Comment on the background quality.
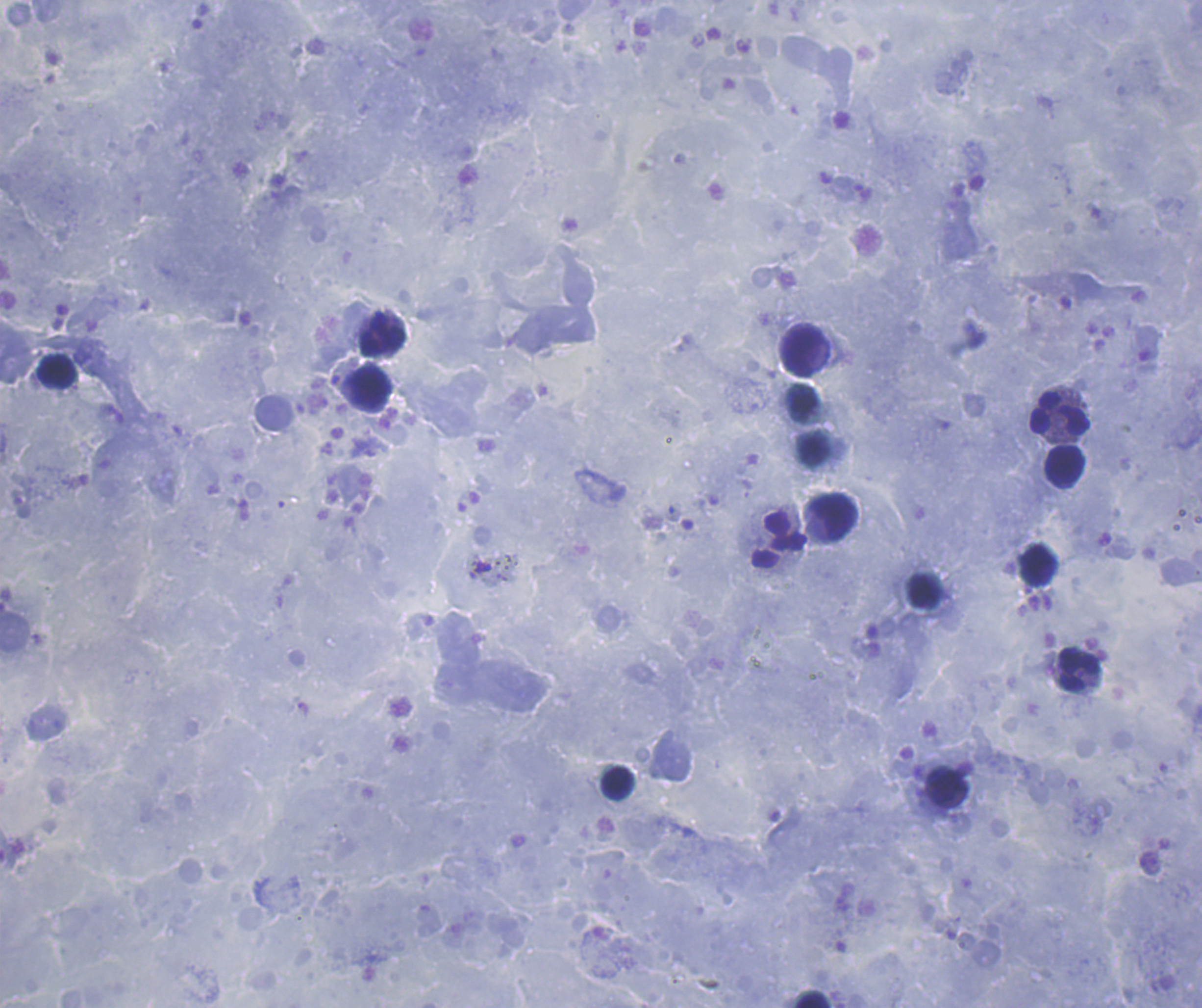

It is good.

Approximate centers as {x, y} in pixels.
Summary:
  - Leukocyte locations: {383, 335}, {803, 351}, {57, 371}, {370, 387}, {1061, 415}, {1065, 467}, {833, 517}, {779, 541}, {1038, 565}, {925, 591}, {1080, 669}, {618, 782}, {947, 787}, {812, 1001}
  - Context: previously used in an actual diagnosis
  - Stain: Romanowsky
  - Magnification: 100x
  - Coloration quality: good
  - Field of view: one from this slide
  - Image size: 1202×1008 pixels
  - Preparation: thick smear of blood
  - Result: no malaria parasites seen